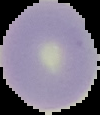

image type = cell region segmented out of the field of view; surrounding area masked to black
result = negative for Plasmodium parasites
preparation = thin blood smear
image size = 100×115 pixels